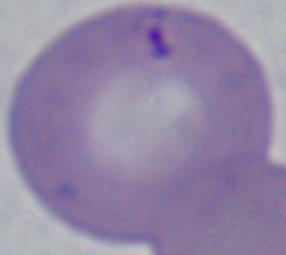

Summary:
  - Magnification: 1000x
  - Modality: micrograph
  - Identification: Babesia